Assess this cell for malaria.
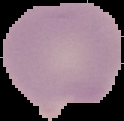

It is uninfected.

preparation = thin blood smear
image size = 124×121 pixels
image type = segmented cell region with the area outside set to black